Outline each blood parasite and name the species.
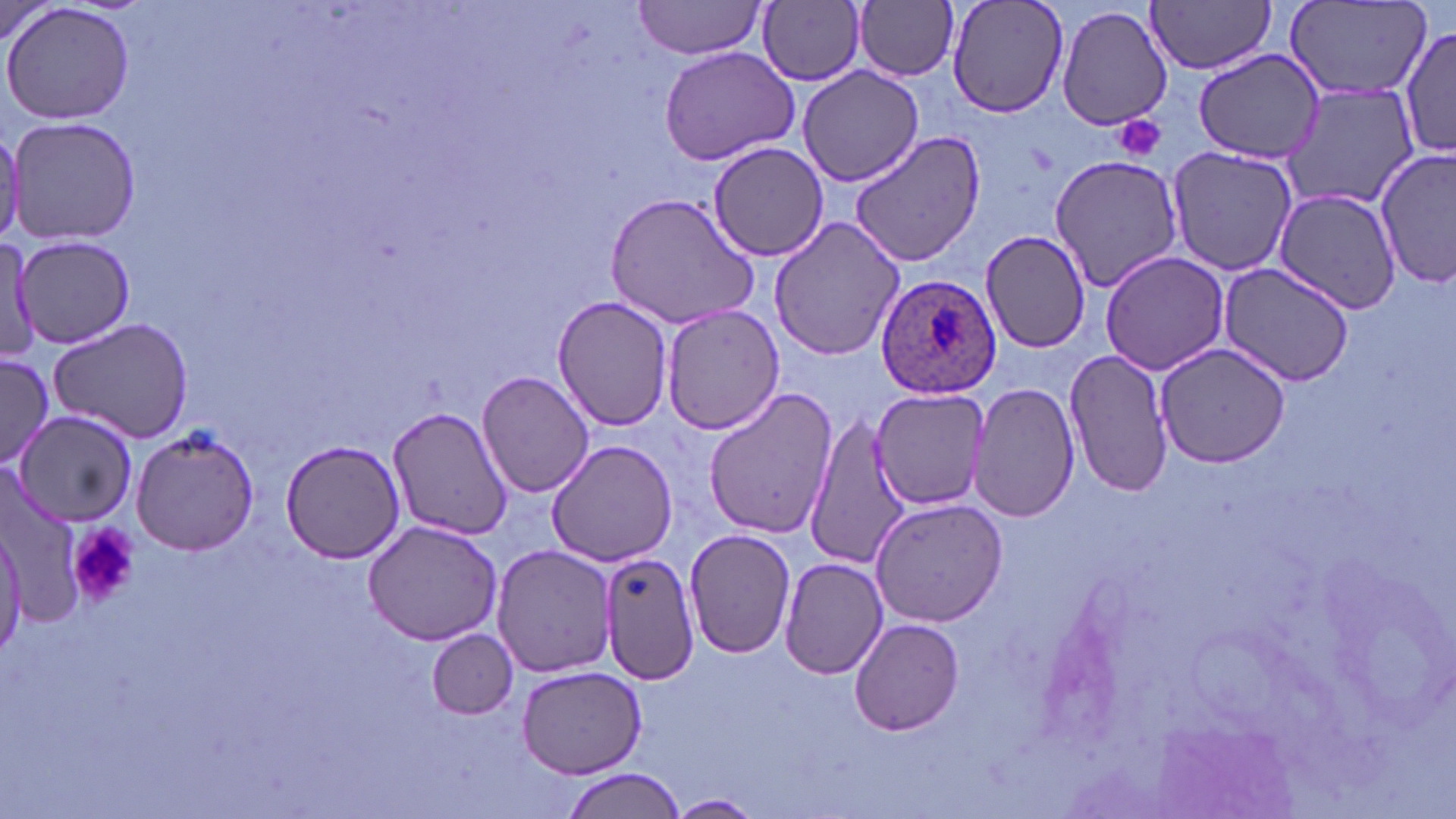

Approximate bounding boxes as (x1, y1, x2, y2) in pixels.
Plasmodium ovale-infected red blood cells: (874, 277, 1002, 401).
No Plasmodium falciparum, Plasmodium malariae, Plasmodium vivax, Babesia divergens, or Trypanosoma brucei observed.

slide-level diagnosis = Plasmodium ovale
magnification = 1000x
image size = 1456×819 pixels
modality = light microscopy
stain = May-Grünwald-Giemsa
uninfected red blood cell locations = approximate bounding boxes as (x1, y1, x2, y2) in pixels: (947, 0, 1069, 119), (1148, 0, 1277, 74), (2, 1, 136, 127), (633, 1, 770, 60), (759, 1, 866, 86), (854, 1, 960, 80), (1286, 2, 1431, 98), (1057, 3, 1173, 131), (1399, 22, 1454, 164), (659, 46, 800, 164), (1193, 50, 1328, 163), (797, 65, 924, 188), (1284, 84, 1420, 211), (7, 117, 143, 247), (0, 125, 24, 250), (849, 131, 986, 266), (707, 142, 830, 262), (1164, 144, 1298, 276), (1374, 146, 1455, 288), (1048, 155, 1182, 289), (1275, 188, 1400, 314), (604, 192, 759, 330), (768, 215, 906, 362), (979, 229, 1091, 354), (13, 234, 136, 349), (0, 237, 38, 366), (1100, 250, 1229, 376), (1216, 261, 1355, 388), (552, 295, 673, 430), (659, 304, 785, 435), (47, 317, 194, 444), (1154, 343, 1293, 468), (1064, 348, 1172, 499), (0, 352, 54, 473), (476, 371, 594, 499), (969, 380, 1079, 523), (703, 388, 838, 539), (871, 389, 989, 512), (384, 405, 514, 542), (14, 411, 139, 527), (803, 413, 913, 573), (130, 427, 261, 553), (279, 439, 408, 565), (546, 440, 681, 568), (869, 497, 1006, 627), (363, 518, 505, 646), (0, 523, 25, 656), (683, 528, 796, 658), (491, 544, 620, 677), (597, 550, 701, 684), (779, 557, 888, 680), (849, 615, 966, 737), (426, 629, 519, 718), (516, 664, 649, 780), (562, 767, 684, 819), (665, 793, 767, 817)
field of view = one of a larger specimen
platelet locations = approximate bounding boxes as (x1, y1, x2, y2) in pixels: (1115, 116, 1167, 163), (68, 520, 139, 609)
preparation = thin blood film